Report the malaria status of this cell.
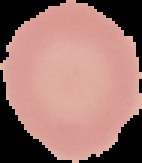

It is uninfected.

Summary:
  - Image size: 142×163 pixels
  - Image type: segmented cell region on a black background
  - Preparation: thin blood film